Mark where platelets are.
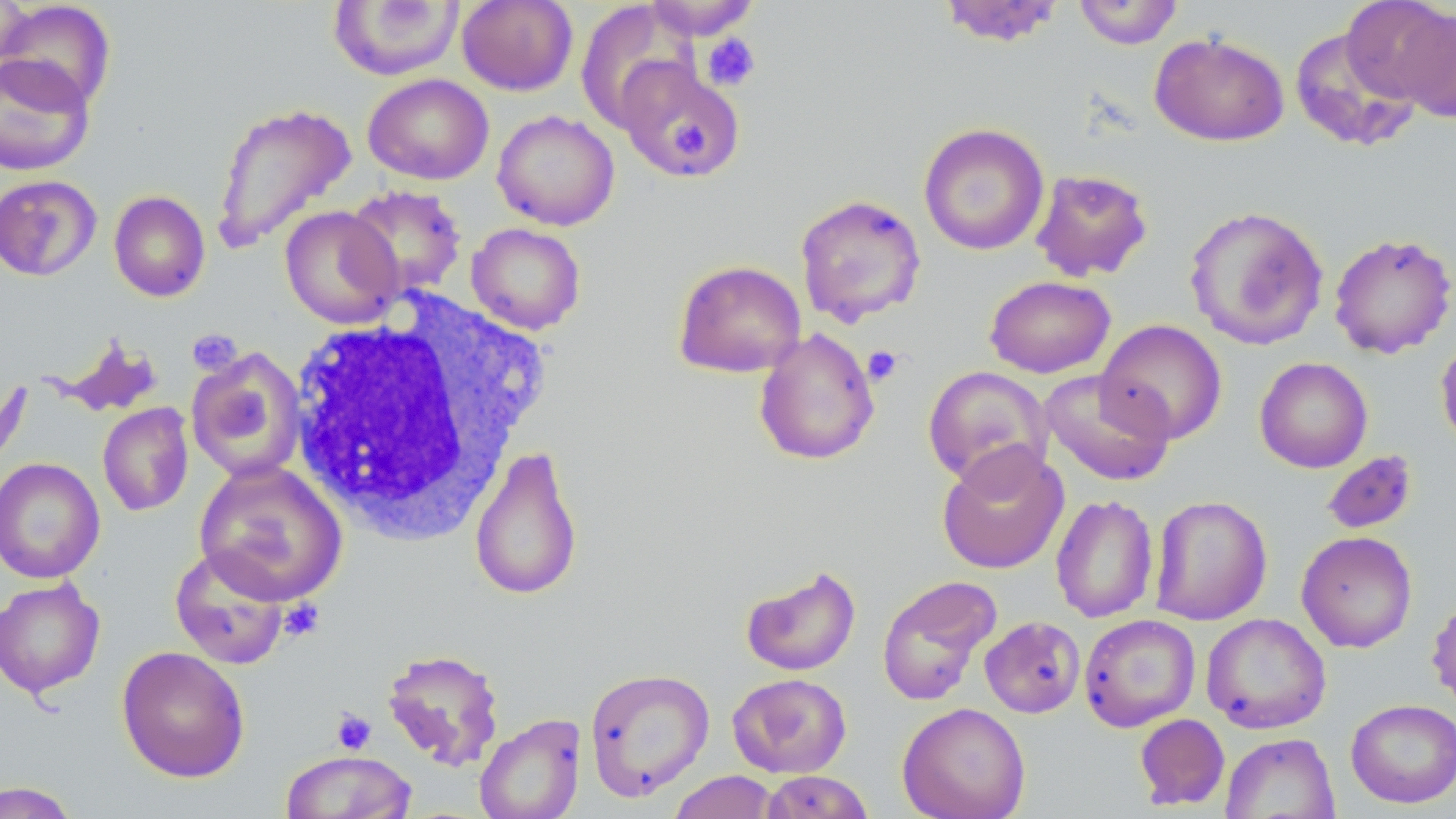

Approximate bounding boxes as [x1, y1, x2, y2] in pixels.
Platelets: [701, 33, 761, 91], [671, 122, 709, 159], [186, 329, 243, 377], [862, 345, 903, 387], [279, 600, 324, 641], [331, 708, 377, 755].

Summary:
  - Uninfected red blood cell locations: [0, 0, 33, 76], [456, 0, 578, 96], [643, 0, 763, 41], [937, 0, 1064, 47], [1072, 0, 1183, 49], [1341, 0, 1454, 108], [0, 1, 117, 111], [328, 1, 465, 81], [574, 2, 696, 132], [1290, 25, 1424, 154], [1150, 32, 1289, 146], [0, 53, 95, 176], [614, 58, 745, 180], [362, 74, 494, 184], [211, 101, 357, 253], [492, 110, 620, 231], [918, 122, 1050, 256], [1030, 169, 1154, 282], [0, 174, 102, 281], [344, 184, 467, 299], [108, 190, 210, 302], [794, 194, 927, 328], [279, 205, 402, 329], [1184, 205, 1329, 350], [466, 222, 586, 335], [1328, 232, 1456, 359], [672, 259, 807, 378], [984, 275, 1116, 379], [1096, 319, 1229, 444], [754, 328, 880, 466], [1435, 334, 1456, 454], [54, 336, 165, 418], [186, 347, 308, 482], [1254, 356, 1373, 473], [922, 365, 1055, 489], [1040, 368, 1176, 487], [97, 402, 194, 517], [936, 442, 1070, 575], [468, 443, 584, 602], [1321, 450, 1418, 536], [0, 457, 105, 583], [194, 458, 348, 605], [1050, 494, 1159, 624], [1149, 495, 1273, 625], [1296, 531, 1418, 653], [169, 545, 291, 669], [739, 564, 861, 676], [876, 574, 1001, 706], [0, 578, 106, 699], [1426, 591, 1456, 715], [1200, 613, 1331, 733], [1079, 614, 1201, 732], [980, 616, 1085, 718], [116, 646, 250, 783], [381, 647, 505, 770], [584, 667, 715, 801], [727, 673, 852, 778], [1345, 698, 1456, 808], [897, 702, 1030, 819], [474, 713, 586, 819], [1134, 713, 1230, 811], [1221, 732, 1340, 819], [280, 750, 416, 818], [667, 770, 782, 819], [761, 770, 875, 818], [0, 781, 83, 819]
  - White blood cell locations: [283, 293, 551, 542]
  - Slide-level diagnosis: negative for blood parasites
  - Magnification: 1000x
  - Stain: May-Grünwald-Giemsa
  - Modality: light microscopy
  - Preparation: thin blood film
  - Field of view: single
  - Image size: 1456×819 pixels